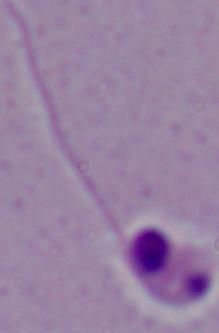

{
  "magnification": "1000x",
  "modality": "photomicrograph",
  "identification": "Leishmania"
}